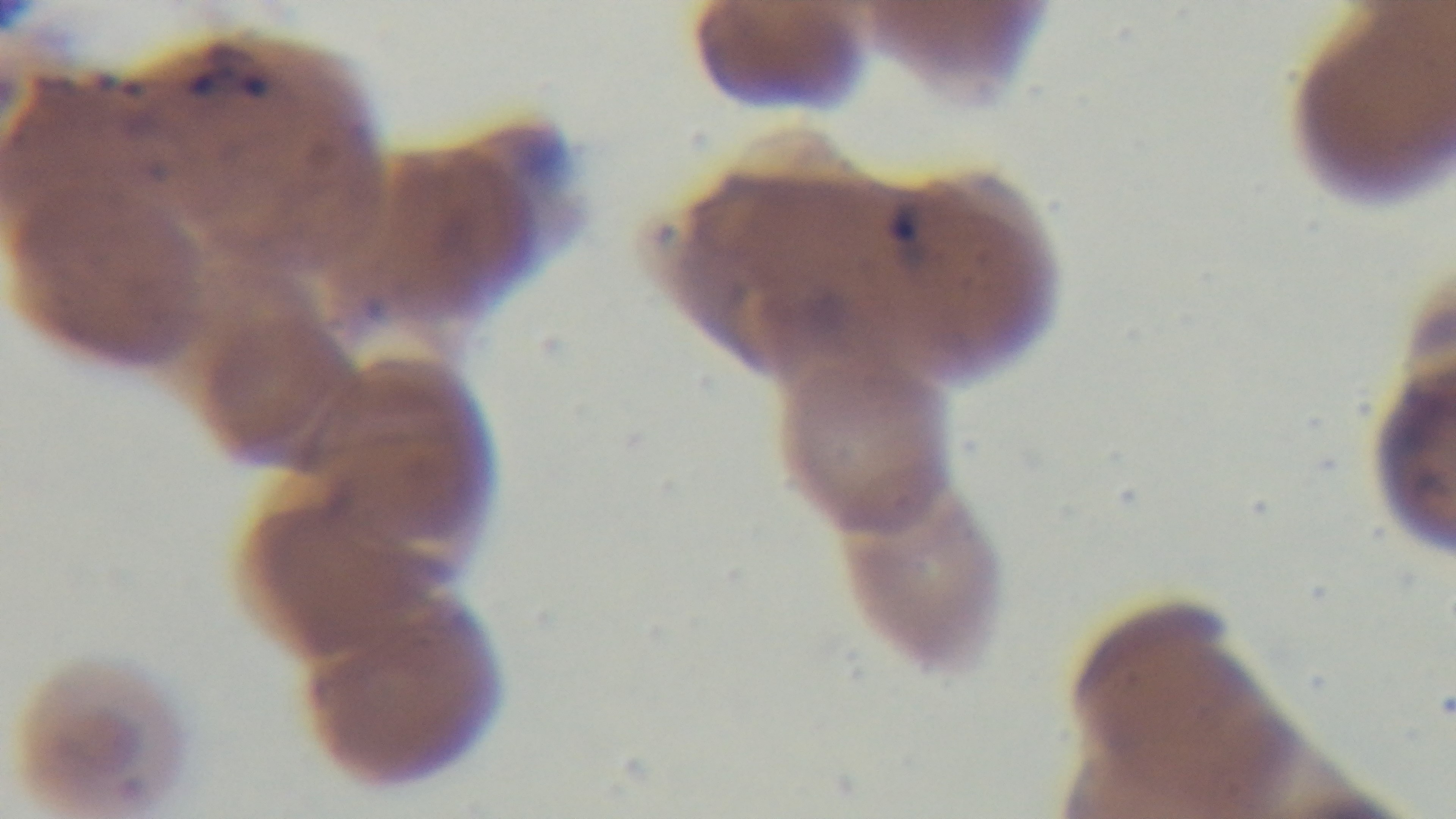

Preparation: thin blood film. Single field of view. Mounted 4K digital camera. Malaria status: infected. 100x oil-immersion objective. Giemsa stain. Photomicrograph.